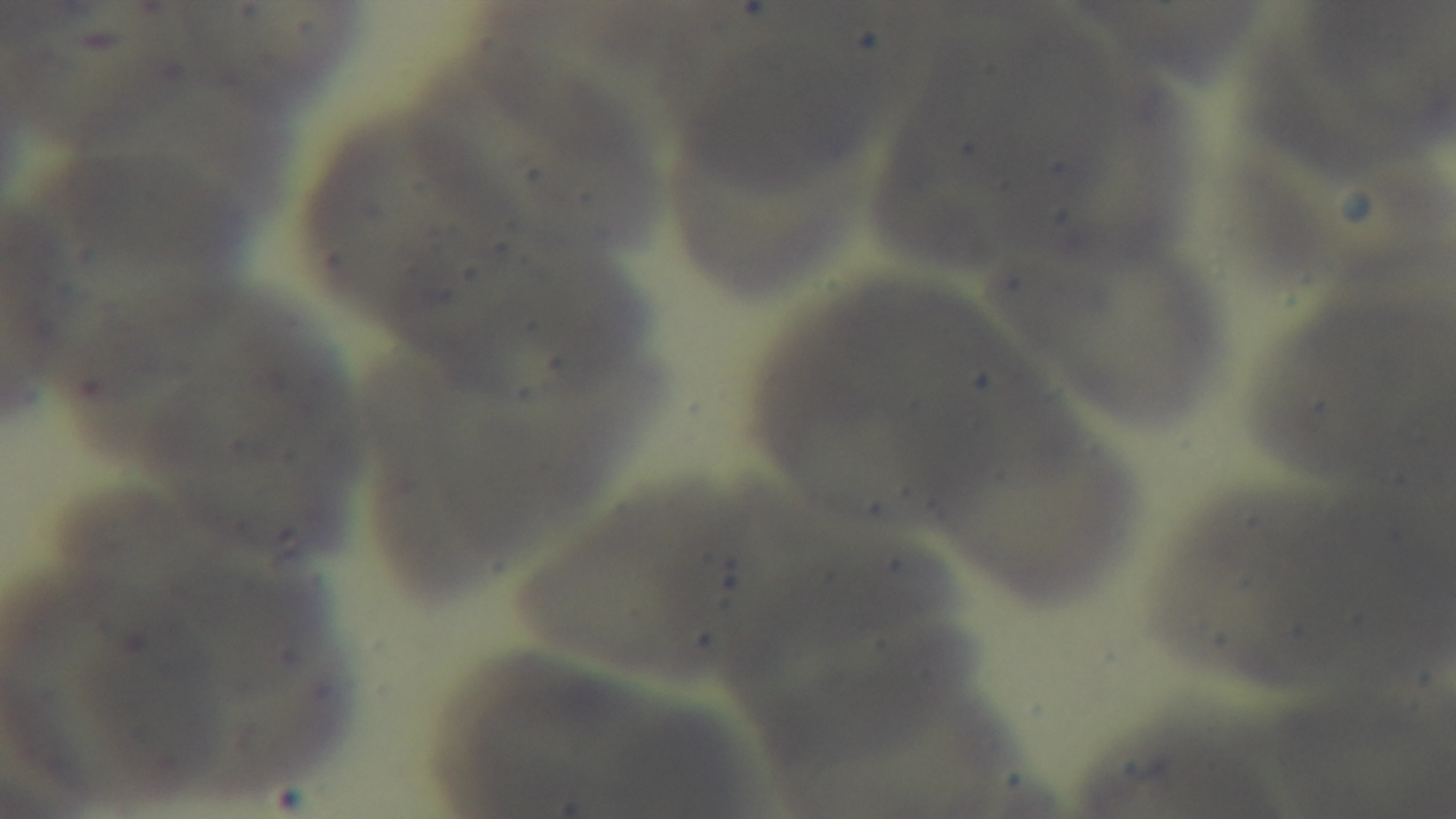
Summary:
  - Objective: 100x oil immersion
  - Capture: mounted 4K digital camera
  - Stain: Giemsa
  - Modality: light microscopy
  - Preparation: thin blood film
  - Malaria status: uninfected
  - Field of view: single